Assess this cell for malaria.
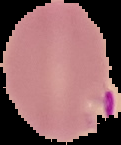
It is parasitized.

preparation = thin blood film
image size = 121×145 pixels
image type = segmented cell region on a black background